Identify the blood parasite species.
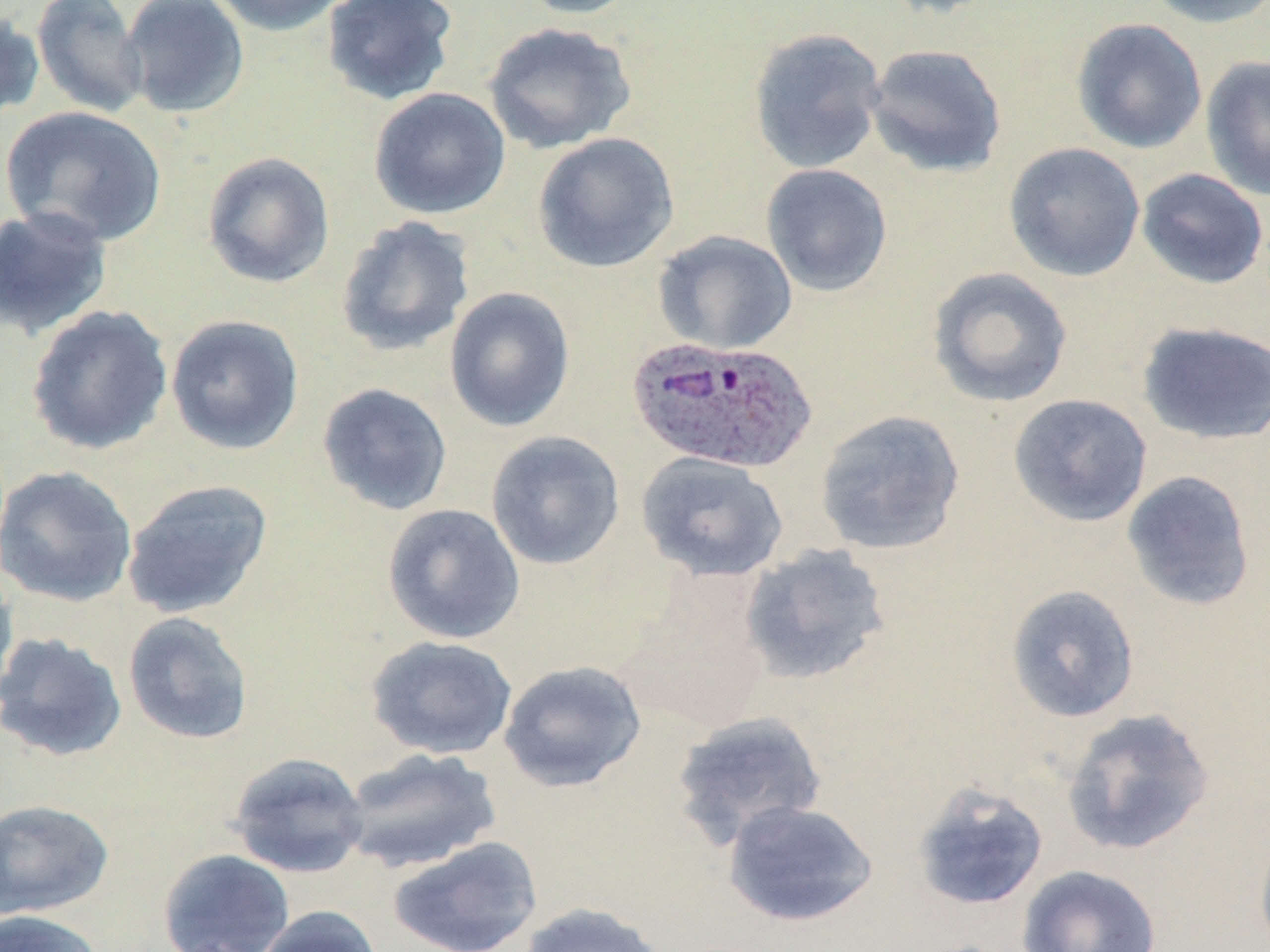
Plasmodium ovale.

Summary:
  - Coordinate format: approximate bounding boxes as (x1,y1)-(x2,y2) corner pairs in pixels
  - Uninfected red blood cell locations: (30,0)-(149,119), (120,0)-(250,119), (207,0)-(351,36), (321,0)-(459,106), (514,0)-(643,20), (872,0)-(1005,19), (1142,0)-(1270,28), (0,8)-(45,123), (1071,17)-(1207,154), (482,22)-(636,154), (747,27)-(887,174), (865,43)-(1008,178), (1200,55)-(1270,201), (369,87)-(511,220), (0,105)-(168,248), (532,131)-(680,273), (1003,142)-(1146,282), (201,151)-(335,289), (761,163)-(893,297), (1136,167)-(1269,289), (0,204)-(113,339), (334,215)-(475,359), (653,230)-(797,355), (927,266)-(1075,408), (444,286)-(576,432), (26,304)-(174,456), (165,314)-(305,456), (1135,321)-(1269,445), (316,382)-(453,516), (1008,393)-(1153,527), (814,409)-(966,555), (485,431)-(626,571), (635,452)-(790,582), (0,465)-(137,607), (1121,470)-(1256,611), (121,478)-(274,619), (382,503)-(525,644), (739,543)-(893,686), (0,557)-(19,700), (623,579)-(773,733), (1005,583)-(1140,723), (122,611)-(255,745), (1,632)-(129,762), (365,635)-(518,760), (498,660)-(647,793), (1061,708)-(1216,856), (669,711)-(828,850), (339,746)-(503,874), (227,751)-(369,879), (911,781)-(1049,912), (0,799)-(114,918), (722,799)-(878,927), (1252,822)-(1270,952), (388,836)-(543,952), (157,848)-(295,952), (1017,864)-(1163,952), (517,902)-(672,952), (255,905)-(383,952), (0,908)-(106,952)
  - Plasmodium ovale-infected red blood cell locations: (624,336)-(818,475)
  - Preparation: thin blood smear
  - Image size: 1270×952 pixels
  - Stain: May-Grünwald-Giemsa
  - Magnification: 1000x
  - Field of view: one of a larger specimen
  - Modality: optical microscopy